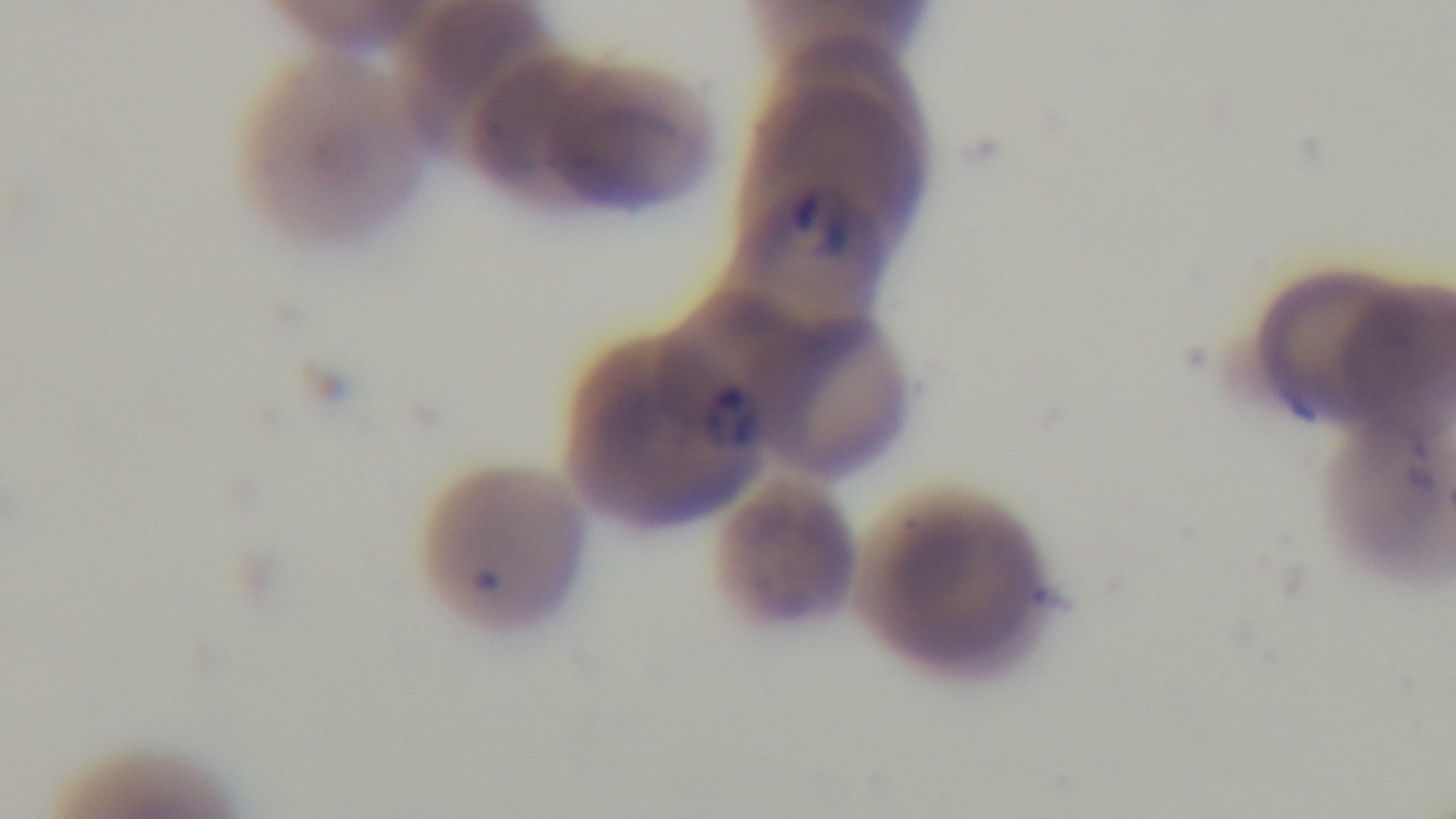

field of view = one from the slide
modality = light microscopy
capture = mounted 4K digital camera
malaria status = positive
objective = 100x oil immersion
preparation = thin
stain = Giemsa